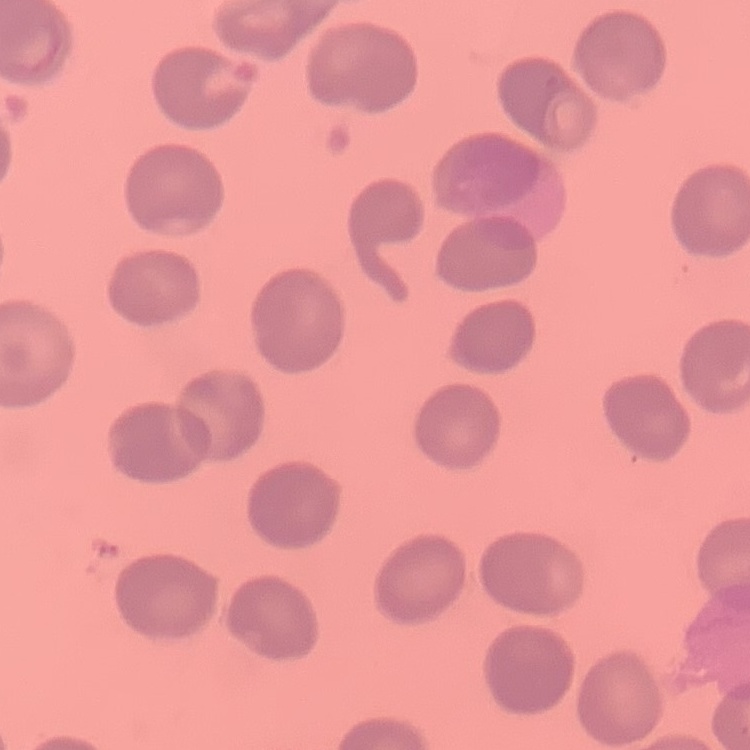

Summary:
  - Red blood cell morphology: no rouleaux formation
  - Stain: Field's or Giemsa
  - Preparation: thin blood smear
  - Image type: one tile cut from a larger photomicrograph